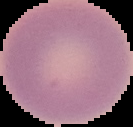 Malaria status: uninfected. Image is 133×127 pixels. The area outside the segmented cell region is set to black. From a thin blood smear.